Locate every Plasmodium vivax-infected red blood cell.
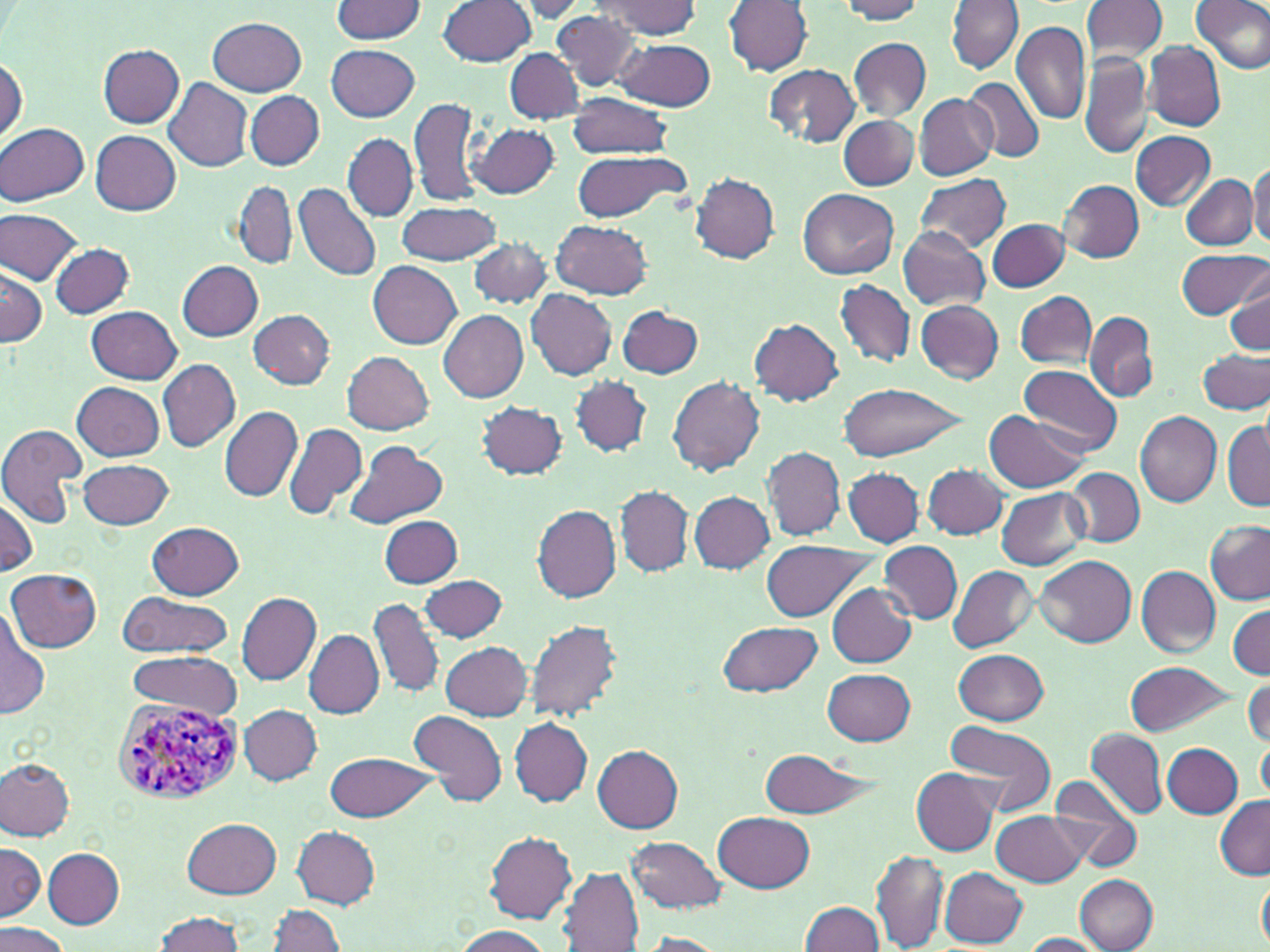

Approximate bounding boxes as (x1, y1, x2, y2) in pixels.
Plasmodium vivax-infected red blood cells: (113, 695, 251, 807).

slide-level diagnosis = Plasmodium vivax
image size = 1270×952 pixels
preparation = thin blood film
stain = May-Grünwald-Giemsa
magnification = 1000x
modality = optical microscopy
field of view = one of a larger specimen
uninfected red blood cell locations = approximate bounding boxes as (x1, y1, x2, y2) in pixels: (332, 0, 426, 42), (724, 0, 812, 76), (836, 0, 929, 23), (946, 0, 1024, 74), (1081, 0, 1168, 63), (1191, 0, 1270, 74), (437, 1, 536, 67), (511, 1, 591, 23), (593, 1, 702, 38), (553, 10, 643, 92), (209, 17, 306, 95), (1012, 22, 1091, 123), (614, 37, 716, 112), (849, 38, 931, 121), (1144, 41, 1226, 130), (97, 44, 185, 127), (327, 44, 419, 121), (504, 48, 585, 125), (1080, 53, 1153, 160), (0, 56, 24, 146), (764, 63, 860, 148), (962, 76, 1046, 163), (163, 79, 253, 172), (246, 92, 325, 169), (566, 93, 672, 160), (914, 94, 998, 180), (409, 96, 484, 209), (837, 114, 919, 192), (0, 122, 89, 207), (469, 123, 558, 198), (90, 130, 182, 214), (1131, 131, 1216, 210), (342, 134, 417, 221), (570, 149, 689, 222), (1247, 160, 1270, 248), (690, 173, 781, 264), (915, 173, 1012, 253), (1180, 173, 1257, 250), (1059, 180, 1144, 262), (294, 181, 382, 282), (233, 183, 296, 267), (798, 188, 899, 278), (395, 201, 503, 266), (1, 207, 85, 283), (987, 218, 1068, 292), (551, 219, 654, 299), (898, 228, 988, 311), (468, 238, 552, 308), (50, 244, 134, 318), (1177, 248, 1267, 319), (179, 260, 262, 341), (369, 261, 462, 350), (1, 266, 46, 348), (1226, 278, 1270, 354), (836, 279, 914, 369), (527, 289, 617, 380), (1015, 291, 1096, 369), (915, 299, 1004, 384), (87, 305, 182, 383), (617, 306, 704, 379), (248, 310, 336, 387), (438, 310, 528, 402), (1084, 310, 1160, 403), (750, 318, 845, 405), (1197, 349, 1270, 414), (343, 351, 434, 434), (157, 360, 240, 452), (1019, 364, 1121, 453), (570, 375, 652, 457), (668, 375, 764, 476), (73, 382, 165, 461), (837, 382, 965, 462), (477, 402, 567, 479), (218, 406, 303, 501), (1134, 409, 1222, 505), (984, 410, 1091, 494), (1222, 421, 1269, 511), (282, 423, 367, 523), (0, 424, 86, 529), (344, 441, 446, 529), (763, 447, 844, 540), (79, 457, 174, 531), (923, 464, 1008, 539), (844, 467, 923, 547), (1066, 468, 1144, 546), (616, 486, 692, 577), (996, 487, 1088, 571), (690, 491, 775, 574), (0, 495, 37, 577), (531, 502, 621, 603), (379, 515, 462, 587), (149, 521, 245, 599), (1203, 521, 1270, 605), (761, 539, 875, 622), (879, 542, 962, 624), (1036, 555, 1137, 645), (1136, 565, 1221, 657), (949, 566, 1036, 653), (8, 568, 100, 652), (419, 574, 508, 643), (826, 582, 916, 666), (118, 591, 231, 658), (237, 591, 321, 687), (369, 597, 444, 698), (1229, 604, 1269, 679), (0, 607, 49, 719), (525, 618, 624, 723), (717, 620, 822, 698), (305, 630, 383, 718), (440, 640, 533, 720), (955, 649, 1050, 725), (129, 650, 241, 718), (1125, 660, 1234, 737), (822, 668, 914, 744), (1244, 678, 1269, 747), (238, 704, 321, 784), (409, 710, 507, 809), (510, 718, 591, 805), (943, 720, 1058, 819), (1085, 729, 1166, 818), (1258, 737, 1270, 803), (1164, 744, 1243, 818), (593, 746, 684, 832), (757, 748, 879, 815), (325, 751, 436, 822), (0, 758, 76, 839), (913, 768, 999, 856), (1048, 777, 1143, 873), (1214, 794, 1270, 878), (992, 810, 1086, 886), (713, 812, 813, 893), (183, 818, 282, 897), (293, 826, 379, 908), (485, 832, 576, 923), (627, 836, 725, 912), (0, 842, 45, 921), (43, 849, 125, 928), (872, 849, 948, 950), (560, 867, 643, 950), (940, 868, 1028, 948), (1258, 872, 1270, 951), (1075, 874, 1158, 952), (800, 902, 885, 951), (267, 903, 346, 952), (151, 911, 246, 951), (0, 922, 73, 952), (451, 926, 553, 952), (633, 932, 727, 952), (1018, 933, 1104, 951)